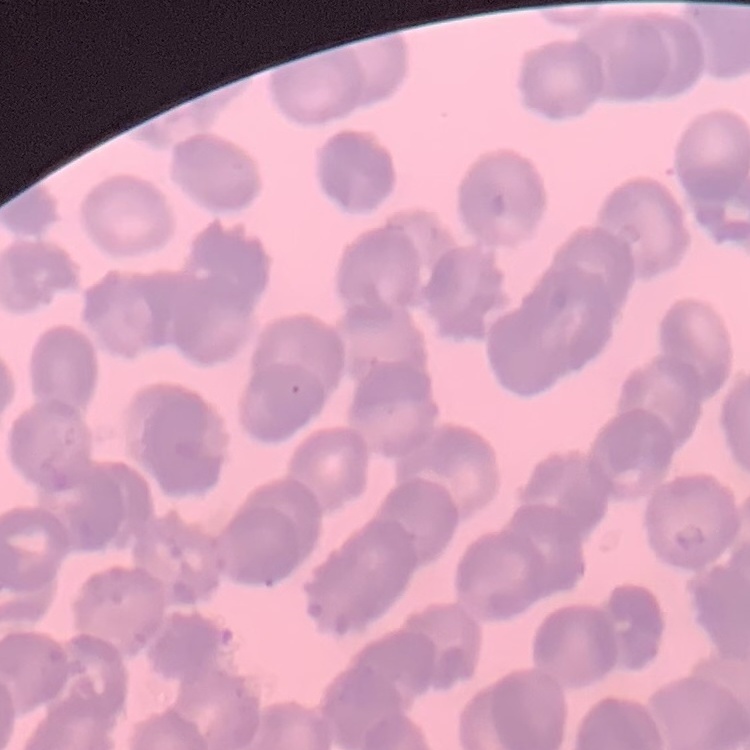

Summary:
  - Red blood cell morphology: rouleaux formation
  - Preparation: thin peripheral smear
  - Image type: square crop of a larger photomicrograph
  - Stain: Field's or Giemsa